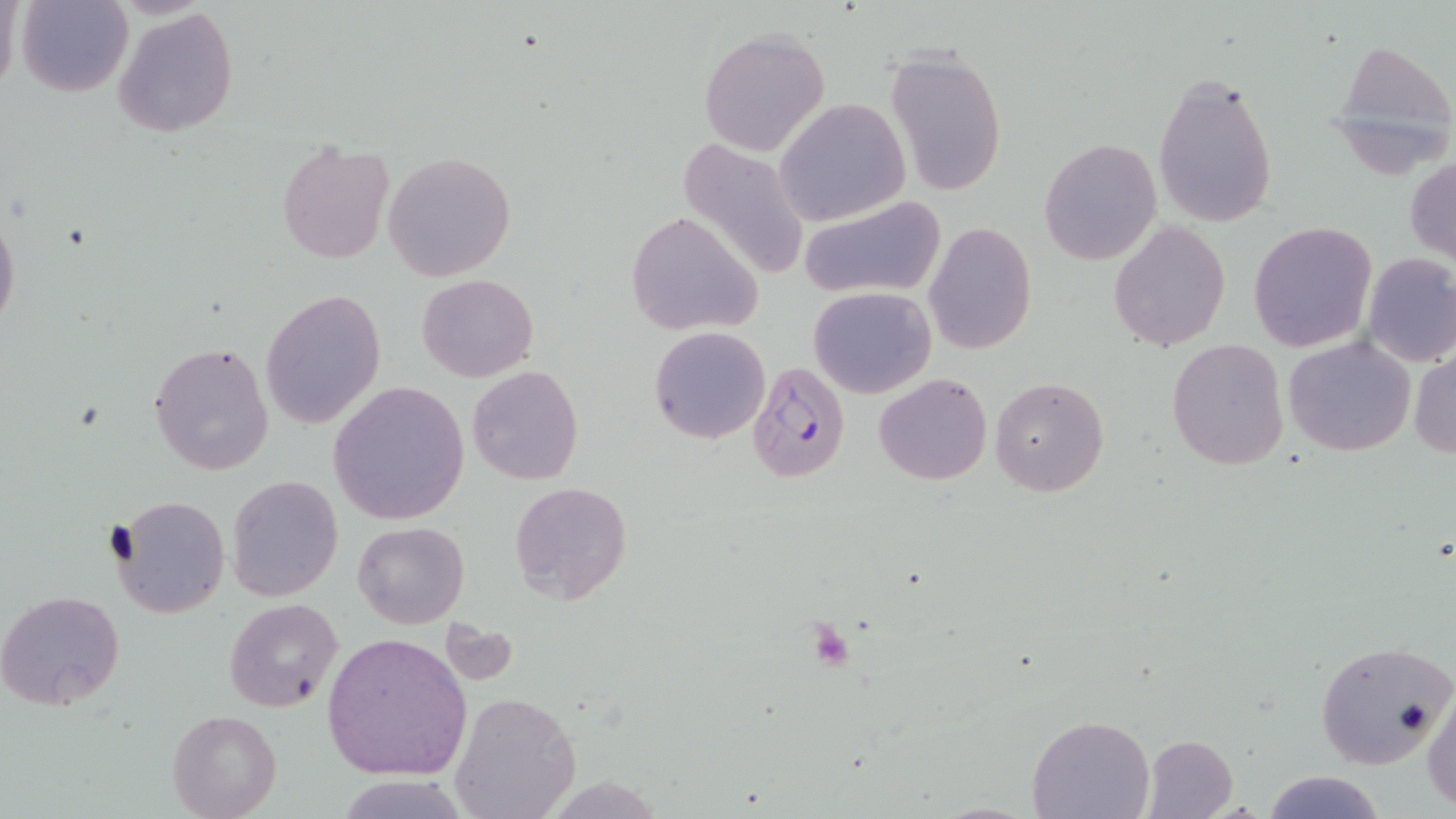
Approximate bounding boxes as named x1/y1/x2/y2 corners in pixels. Uninfected red blood cell locations: (x1=15, y1=0, x2=134, y2=97), (x1=112, y1=7, x2=239, y2=138), (x1=699, y1=29, x2=830, y2=158), (x1=1327, y1=35, x2=1456, y2=178), (x1=885, y1=52, x2=1008, y2=198), (x1=1152, y1=67, x2=1279, y2=229), (x1=776, y1=98, x2=911, y2=225), (x1=675, y1=135, x2=809, y2=285), (x1=1039, y1=138, x2=1162, y2=264), (x1=276, y1=141, x2=394, y2=264), (x1=384, y1=151, x2=516, y2=281), (x1=1406, y1=156, x2=1456, y2=266), (x1=796, y1=198, x2=945, y2=299), (x1=0, y1=207, x2=20, y2=337), (x1=624, y1=210, x2=764, y2=337), (x1=923, y1=220, x2=1036, y2=356), (x1=1108, y1=220, x2=1231, y2=353), (x1=1249, y1=222, x2=1377, y2=354), (x1=1362, y1=253, x2=1456, y2=368), (x1=417, y1=274, x2=538, y2=383), (x1=808, y1=285, x2=936, y2=398), (x1=260, y1=289, x2=385, y2=431), (x1=649, y1=326, x2=770, y2=445), (x1=1284, y1=337, x2=1416, y2=457), (x1=1167, y1=339, x2=1291, y2=471), (x1=149, y1=341, x2=274, y2=476), (x1=1410, y1=351, x2=1456, y2=457), (x1=466, y1=364, x2=584, y2=485), (x1=873, y1=372, x2=993, y2=486), (x1=990, y1=376, x2=1109, y2=497), (x1=329, y1=382, x2=469, y2=525), (x1=227, y1=475, x2=343, y2=602), (x1=508, y1=481, x2=632, y2=603), (x1=112, y1=495, x2=229, y2=618), (x1=353, y1=521, x2=469, y2=628), (x1=0, y1=590, x2=126, y2=710), (x1=223, y1=598, x2=342, y2=712), (x1=438, y1=620, x2=520, y2=687), (x1=320, y1=632, x2=473, y2=781), (x1=1316, y1=640, x2=1455, y2=769), (x1=1423, y1=685, x2=1456, y2=810), (x1=448, y1=690, x2=581, y2=819), (x1=167, y1=710, x2=281, y2=819), (x1=1027, y1=716, x2=1153, y2=819), (x1=1142, y1=735, x2=1241, y2=819), (x1=1260, y1=770, x2=1388, y2=819), (x1=331, y1=774, x2=476, y2=818). Plasmodium falciparum-infected red blood cell locations: (x1=746, y1=361, x2=848, y2=484). Slide-level diagnosis: Plasmodium falciparum. Image is 1456×819 pixels. Captured at 1000x magnification. Thin blood film. Optical microscopy. Single field of view. May-Grünwald-Giemsa-stained preparation.